Name the blood parasite species.
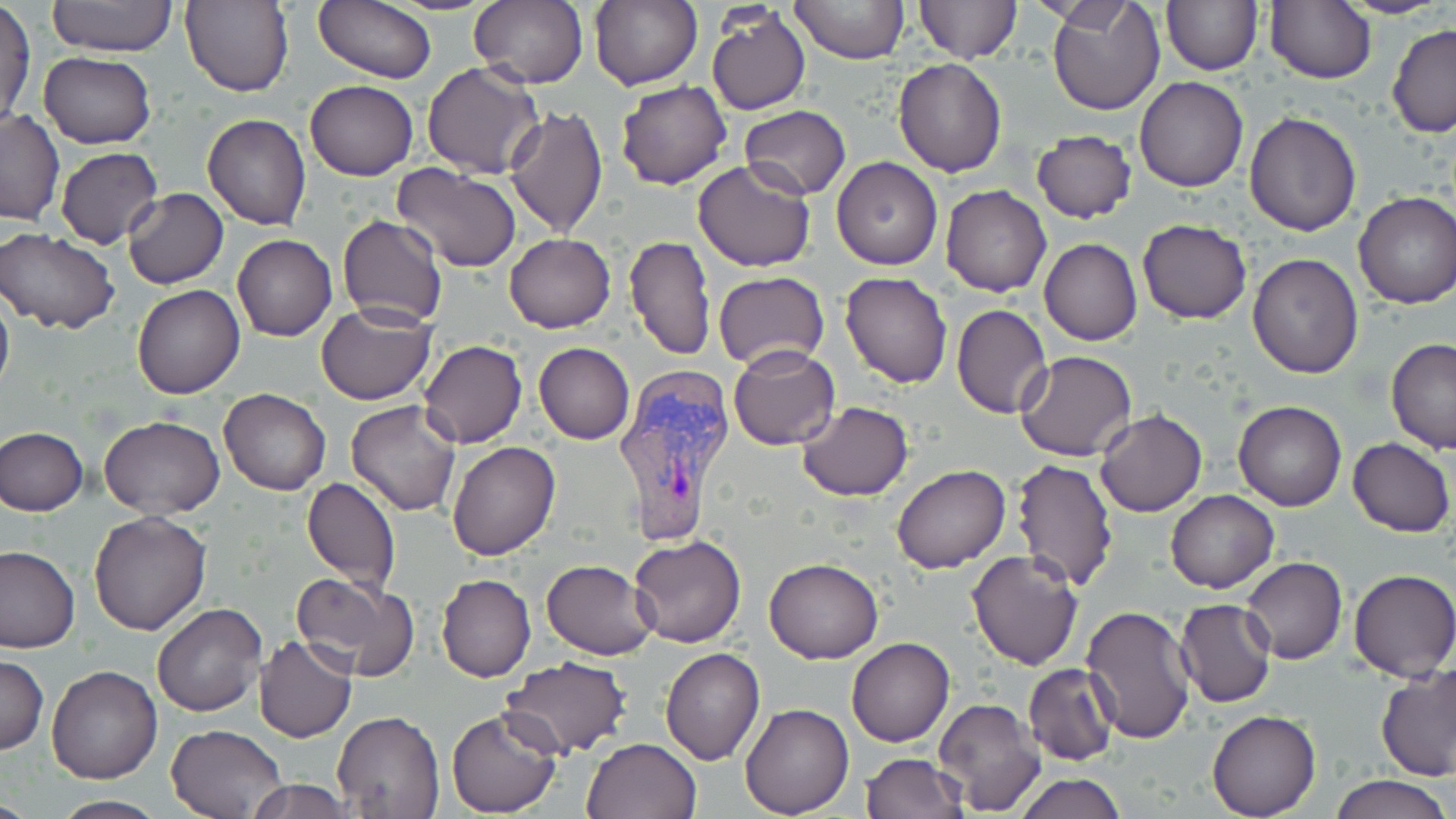

Plasmodium vivax.

modality: optical microscopy
preparation: thin blood film
uninfected_red_blood_cell_locations: 'approximate bounding boxes as (x1,y1)-(x2,y2) corner pairs in pixels: (46,0)-(179,56), (314,0)-(436,83), (387,0)-(501,14), (590,0)-(704,92), (789,0)-(909,66), (915,0)-(1020,63), (1046,0)-(1164,115), (1342,0)-(1450,19), (180,1)-(294,96), (468,1)-(588,88), (1161,1)-(1262,75), (1267,1)-(1375,83), (1,4)-(35,129), (706,7)-(810,117), (1387,22)-(1456,137), (39,52)-(156,150), (893,58)-(1007,177), (422,62)-(545,180), (1133,75)-(1249,192), (305,80)-(418,181), (615,80)-(733,190), (504,104)-(607,237), (738,105)-(852,200), (0,109)-(64,226), (1244,111)-(1362,236), (202,113)-(311,230), (1032,129)-(1136,223), (56,146)-(163,249), (693,158)-(817,273), (831,158)-(943,270), (393,164)-(522,273), (342,178)-(505,313), (940,185)-(1052,297), (122,188)-(228,289), (1352,190)-(1456,308), (337,215)-(449,327), (1137,218)-(1252,324), (0,228)-(119,334), (504,233)-(616,333), (624,234)-(715,360), (233,235)-(338,340), (1039,239)-(1142,346), (1247,252)-(1365,377), (714,271)-(829,371), (840,272)-(952,388), (133,285)-(244,399), (0,289)-(14,403), (314,302)-(437,405), (951,304)-(1054,419), (1385,338)-(1456,454), (418,340)-(527,448), (534,343)-(634,444), (728,343)-(840,450), (1016,350)-(1137,460), (220,388)-(331,495), (797,400)-(914,500), (1233,400)-(1345,511), (347,401)-(460,516), (1095,409)-(1207,517), (99,415)-(224,520), (0,427)-(88,514), (1346,437)-(1455,536), (447,441)-(560,560), (1011,458)-(1118,590), (891,465)-(1011,574), (300,476)-(402,594), (1166,490)-(1280,594), (89,511)-(211,635), (627,535)-(746,648), (0,545)-(78,652), (967,549)-(1084,669), (1242,556)-(1347,664), (764,558)-(883,664), (541,559)-(659,660), (1348,569)-(1456,683), (290,571)-(421,682), (436,573)-(536,683), (1174,598)-(1276,708), (151,602)-(267,717), (1080,604)-(1197,744), (254,635)-(356,742), (847,637)-(955,747), (660,646)-(766,764), (0,654)-(48,755), (500,656)-(630,758), (1022,663)-(1119,765), (1377,664)-(1454,779), (47,665)-(162,783), (932,697)-(1047,817), (740,704)-(853,817), (446,707)-(561,816), (332,709)-(445,818), (1206,710)-(1321,819), (166,723)-(289,818), (581,737)-(702,819), (860,752)-(967,819), (1012,772)-(1128,819), (1329,774)-(1449,819), (245,778)-(354,819), (48,794)-(168,818)'
image_size: 1456×819 pixels
plasmodium_vivax_infected_red_blood_cell_locations: 'approximate bounding boxes as (x1,y1)-(x2,y2) corner pairs in pixels: (612,365)-(737,546)'
stain: May-Grünwald-Giemsa
field_of_view: one of a larger specimen
magnification: 1000x